Locate every Plasmodium parasite.
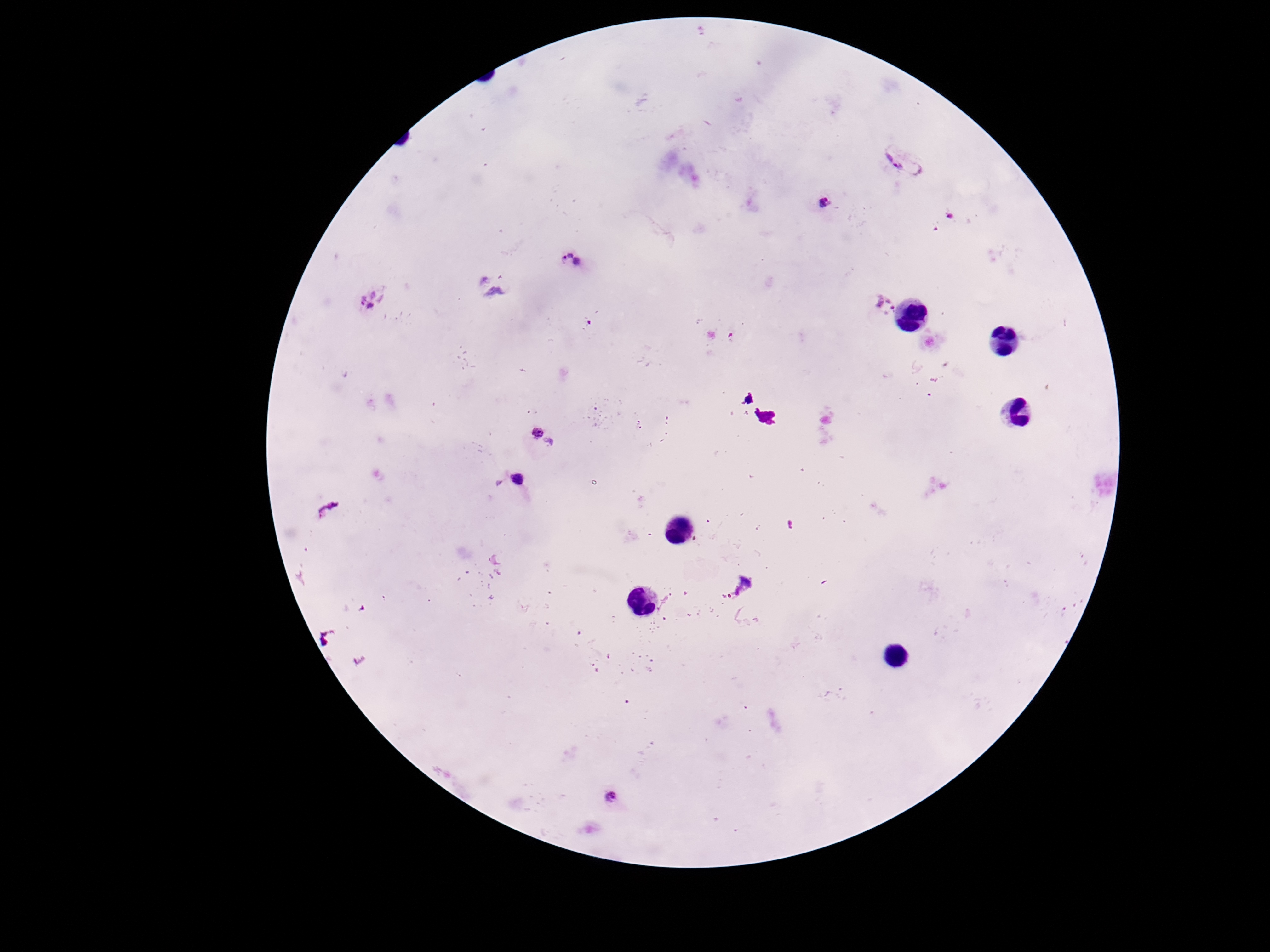
Approximate centers as [x, y] in pixels.
Plasmodium parasites: [904, 162], [826, 204], [571, 259], [374, 300], [885, 305], [539, 441], [513, 485], [327, 509], [610, 798].

preparation = thick peripheral-blood smear
capture = smartphone camera through the microscope eyepiece
image size = 1270×952 pixels
field of view = one from this slide
stain = Giemsa
patient malaria status = positive
magnification = 100x